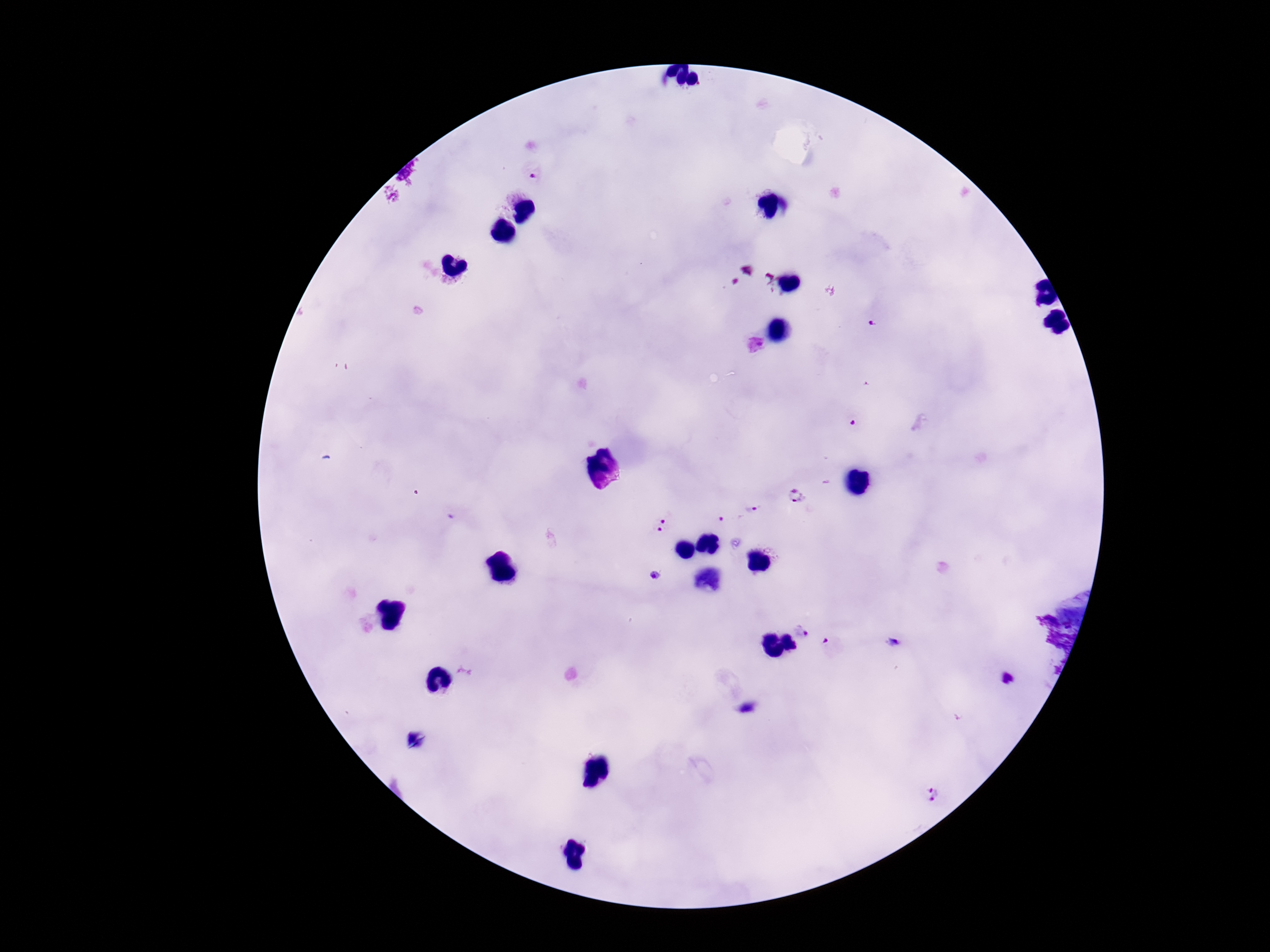
Approximate centers as [x, y] in pixels.
Summary:
  - Plasmodium parasite locations: [535, 173], [872, 325], [796, 497], [751, 509], [664, 514], [723, 519], [659, 533], [655, 574], [805, 628], [833, 647], [1008, 679], [932, 797]
  - Stain: Giemsa
  - Preparation: thick blood film
  - Patient malaria status: infected
  - Field of view: single
  - Magnification: 100x
  - Image size: 1270×952 pixels
  - Capture: smartphone camera through the microscope eyepiece